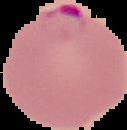
Summary:
  - Preparation: thin blood smear
  - Image size: 127×130 pixels
  - Result: Plasmodium parasites detected
  - Image type: segmented cell region on a black background